Point out cells.
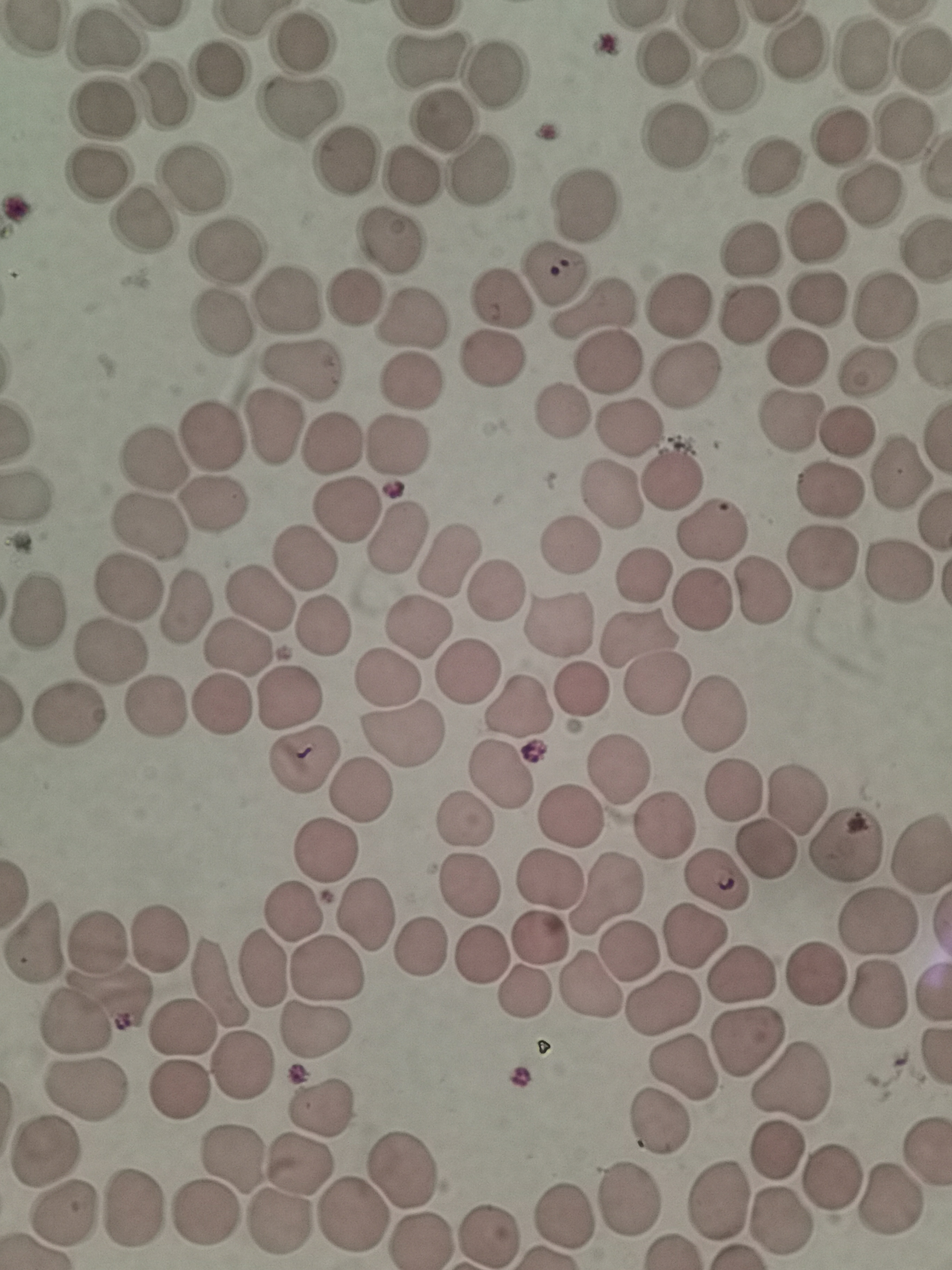
Approximate object centers, in pixels from the top-left corner.
Cells: (x=102, y=42), (x=298, y=42), (x=798, y=48), (x=664, y=56), (x=923, y=57), (x=862, y=58), (x=428, y=60), (x=221, y=69), (x=498, y=77), (x=728, y=82), (x=166, y=93), (x=297, y=108), (x=104, y=110), (x=440, y=118), (x=905, y=133), (x=678, y=136), (x=837, y=140), (x=345, y=159), (x=770, y=166), (x=479, y=168), (x=412, y=173), (x=98, y=175), (x=192, y=178), (x=868, y=196), (x=590, y=204), (x=140, y=222), (x=811, y=234), (x=390, y=241), (x=749, y=250), (x=222, y=253), (x=552, y=273), (x=355, y=297), (x=502, y=297), (x=817, y=299), (x=290, y=301), (x=882, y=303), (x=678, y=306), (x=594, y=309), (x=414, y=321), (x=742, y=322), (x=218, y=324), (x=800, y=356), (x=489, y=358), (x=606, y=365), (x=305, y=368), (x=869, y=371), (x=685, y=374), (x=406, y=382), (x=563, y=409), (x=792, y=419), (x=627, y=426), (x=849, y=429), (x=272, y=430), (x=211, y=437), (x=327, y=444), (x=393, y=447), (x=155, y=460), (x=900, y=472), (x=670, y=474), (x=829, y=492), (x=612, y=494), (x=346, y=506), (x=210, y=509), (x=711, y=525), (x=149, y=528), (x=394, y=538), (x=569, y=541), (x=304, y=556), (x=450, y=557), (x=826, y=561), (x=896, y=571), (x=646, y=575), (x=125, y=586), (x=495, y=591), (x=762, y=592), (x=261, y=597), (x=698, y=598), (x=182, y=607), (x=36, y=608), (x=320, y=623), (x=560, y=624), (x=423, y=626), (x=640, y=638), (x=239, y=649), (x=111, y=651), (x=473, y=672), (x=386, y=678), (x=658, y=682), (x=581, y=685), (x=288, y=693), (x=517, y=703), (x=226, y=706), (x=151, y=707), (x=713, y=712), (x=71, y=717), (x=398, y=734), (x=302, y=758), (x=619, y=769), (x=502, y=773), (x=734, y=789), (x=360, y=790), (x=795, y=795), (x=571, y=815), (x=468, y=819), (x=664, y=827), (x=845, y=846), (x=327, y=849), (x=765, y=850), (x=917, y=858), (x=547, y=879), (x=718, y=882), (x=471, y=886), (x=604, y=891), (x=291, y=910), (x=363, y=914), (x=878, y=920), (x=697, y=937), (x=101, y=939), (x=161, y=940), (x=544, y=941), (x=39, y=943), (x=423, y=950), (x=627, y=951), (x=481, y=952), (x=264, y=964), (x=323, y=969), (x=815, y=974), (x=741, y=975), (x=219, y=984), (x=594, y=988), (x=876, y=992), (x=108, y=994), (x=524, y=994), (x=665, y=1006), (x=76, y=1019), (x=182, y=1027), (x=313, y=1030), (x=747, y=1042), (x=245, y=1063), (x=684, y=1069), (x=796, y=1081), (x=182, y=1090), (x=85, y=1092), (x=323, y=1104), (x=661, y=1125), (x=780, y=1149), (x=45, y=1154), (x=237, y=1158), (x=301, y=1163), (x=401, y=1170), (x=833, y=1179), (x=629, y=1197), (x=719, y=1200), (x=889, y=1200), (x=135, y=1208), (x=206, y=1213), (x=66, y=1214), (x=562, y=1215), (x=352, y=1217), (x=282, y=1222), (x=784, y=1222), (x=489, y=1235), (x=422, y=1238).

Image is 952×1270 pixels. Giemsa-stained preparation. Thin blood film. Photographed with a smartphone camera at the microscope eyepiece. Single field of view.